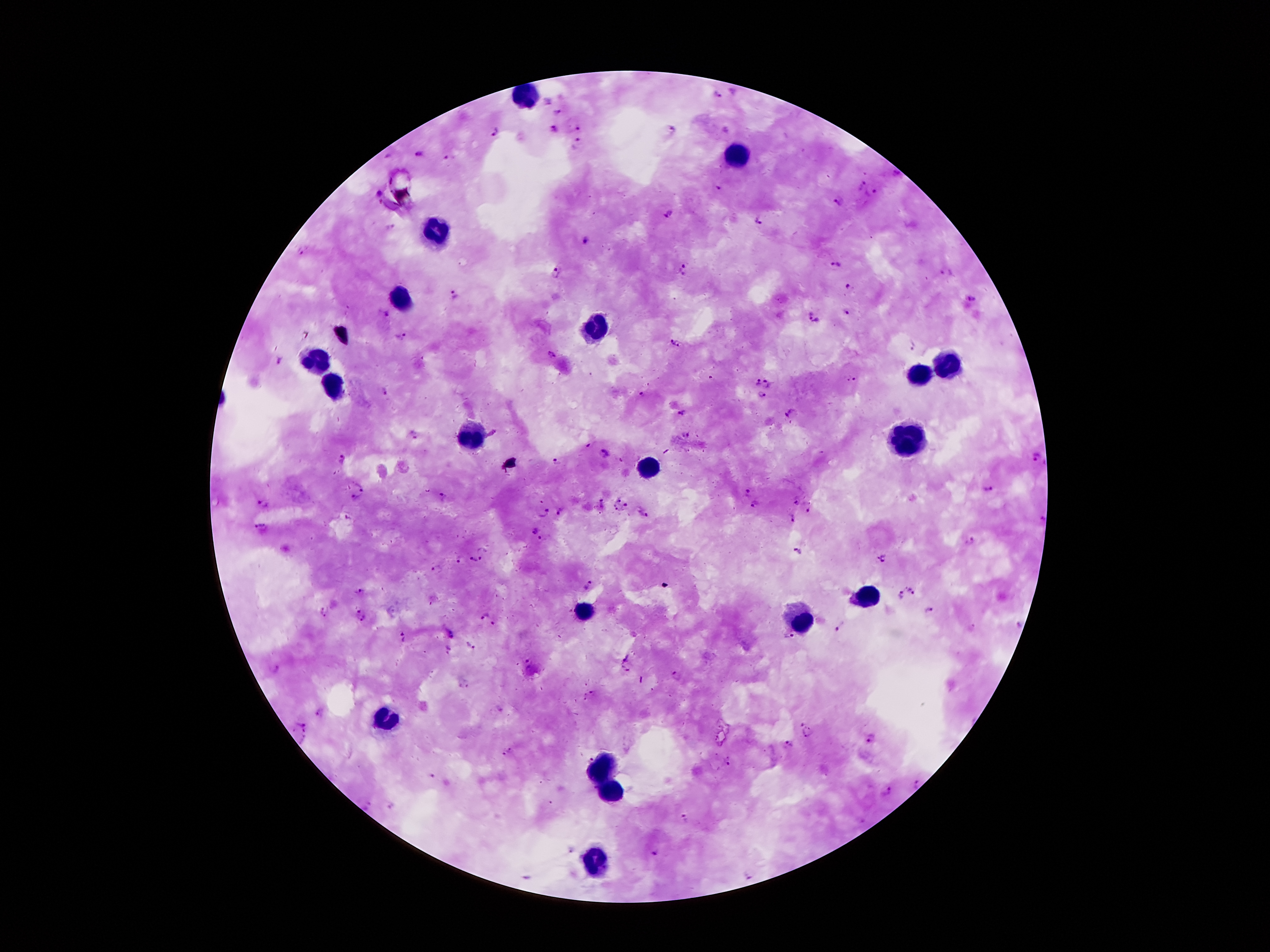 Approximate centers as {x, y} in pixels. Plasmodium parasite locations: {717, 96}, {558, 112}, {580, 125}, {554, 130}, {670, 130}, {495, 133}, {578, 143}, {419, 154}, {446, 158}, {860, 184}, {872, 193}, {838, 200}, {669, 214}, {763, 223}, {391, 226}, {587, 240}, {303, 252}, {838, 265}, {684, 270}, {557, 273}, {949, 273}, {850, 286}, {452, 296}, {970, 299}, {847, 311}, {809, 314}, {387, 315}, {401, 337}, {674, 345}, {914, 348}, {551, 357}, {279, 360}, {855, 379}, {755, 382}, {768, 384}, {384, 392}, {644, 394}, {761, 395}, {684, 413}, {791, 416}, {688, 432}, {589, 444}, {605, 453}, {342, 460}, {558, 460}, {1037, 460}, {361, 484}, {990, 488}, {748, 492}, {444, 497}, {357, 499}, {619, 499}, {797, 501}, {264, 502}, {754, 505}, {625, 506}, {810, 508}, {614, 509}, {561, 512}, {544, 513}, {642, 514}, {793, 518}, {261, 528}, {536, 530}, {540, 540}, {973, 541}, {484, 551}, {798, 554}, {883, 559}, {472, 561}, {438, 568}, {589, 586}, {913, 590}, {360, 592}, {899, 596}, {324, 612}, {929, 612}, {483, 616}, {362, 619}, {839, 626}, {449, 632}, {786, 636}, {404, 638}, {470, 645}, {448, 649}, {528, 660}, {677, 677}, {594, 695}, {304, 721}, {809, 732}, {871, 740}, {790, 744}, {508, 751}, {430, 775}, {915, 784}, {887, 792}, {393, 805}, {683, 820}, {655, 853}, {748, 874}. Leukocyte locations: {526, 97}, {736, 156}, {440, 236}, {402, 299}, {599, 326}, {316, 362}, {941, 362}, {920, 378}, {335, 385}, {473, 433}, {908, 441}, {647, 469}, {866, 597}, {582, 614}, {799, 620}, {385, 718}, {601, 767}, {612, 794}, {595, 865}. Thick blood film. 100x magnification. Patient malaria status: infected with Plasmodium falciparum. Giemsa stain. Smartphone photograph taken through the microscope eyepiece. Image is 1270×952 pixels. Single field of view.